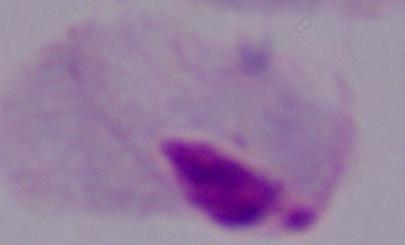

A trichomonad is seen. Photomicrograph. 1000x magnification.